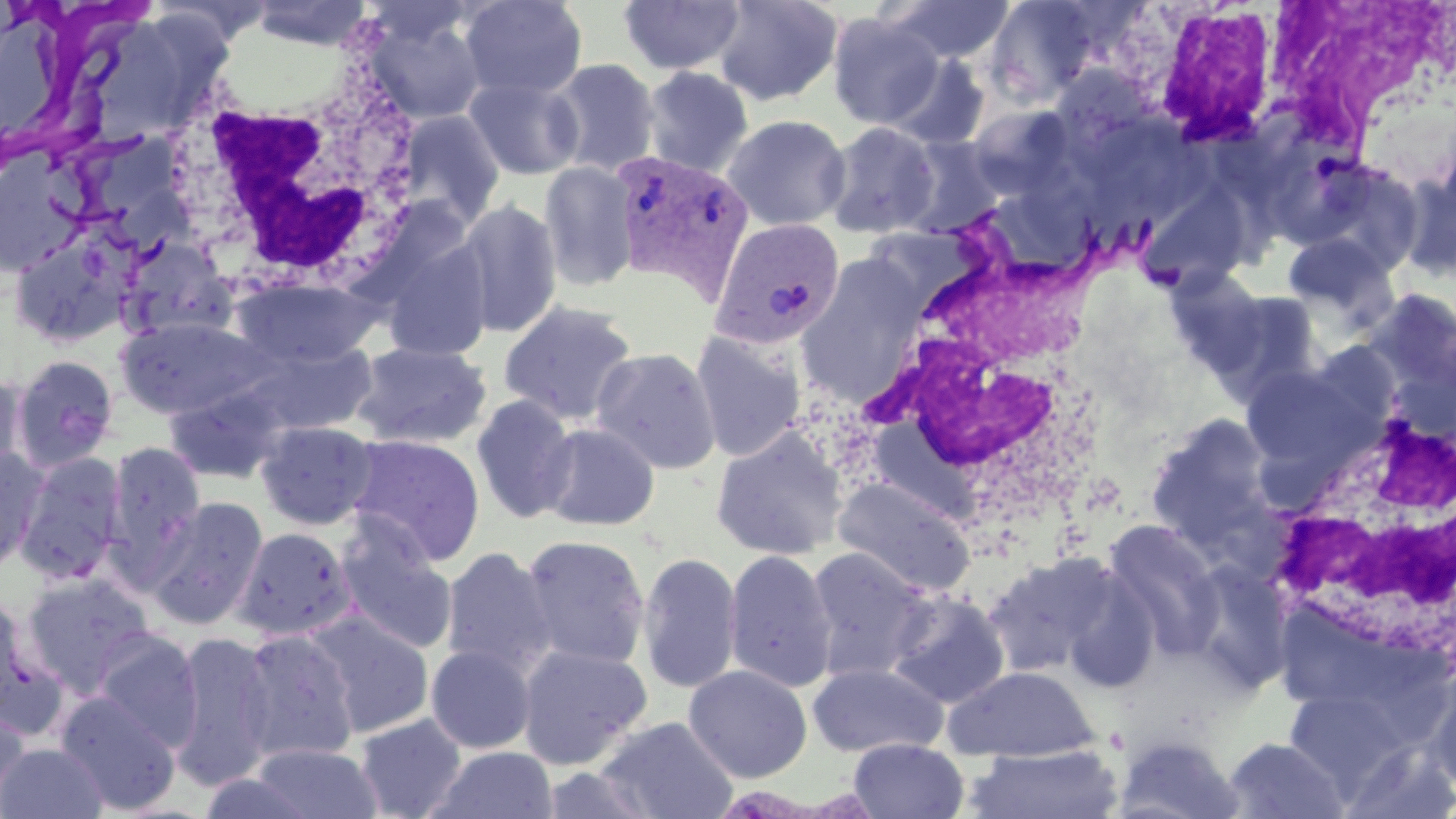 Approximate bounding boxes as named x1/y1/x2/y2 corners in pixels. Plasmodium vivax-infected red blood cell locations: (x1=610, y1=149, x2=755, y2=299), (x1=708, y1=217, x2=845, y2=352). White blood cell locations: (x1=1270, y1=3, x2=1453, y2=167), (x1=1118, y1=4, x2=1285, y2=151), (x1=159, y1=51, x2=423, y2=303), (x1=861, y1=226, x2=1112, y2=525), (x1=1261, y1=409, x2=1455, y2=662). Uninfected red blood cell locations: (x1=251, y1=0, x2=370, y2=50), (x1=460, y1=0, x2=587, y2=101), (x1=618, y1=0, x2=745, y2=76), (x1=713, y1=0, x2=844, y2=106), (x1=885, y1=0, x2=1015, y2=64), (x1=984, y1=1, x2=1104, y2=106), (x1=362, y1=9, x2=487, y2=125), (x1=3, y1=11, x2=70, y2=140), (x1=826, y1=12, x2=945, y2=130), (x1=84, y1=18, x2=184, y2=141), (x1=886, y1=54, x2=991, y2=151), (x1=547, y1=58, x2=661, y2=176), (x1=640, y1=65, x2=754, y2=179), (x1=464, y1=76, x2=584, y2=180), (x1=968, y1=105, x2=1076, y2=199), (x1=398, y1=110, x2=505, y2=226), (x1=722, y1=114, x2=850, y2=231), (x1=823, y1=122, x2=941, y2=239), (x1=903, y1=136, x2=1006, y2=237), (x1=3, y1=140, x2=92, y2=277), (x1=1308, y1=159, x2=1427, y2=276), (x1=539, y1=160, x2=639, y2=291), (x1=1135, y1=179, x2=1256, y2=295), (x1=453, y1=200, x2=563, y2=338), (x1=9, y1=231, x2=133, y2=347), (x1=1283, y1=233, x2=1397, y2=325), (x1=116, y1=237, x2=237, y2=342), (x1=382, y1=238, x2=493, y2=363), (x1=232, y1=276, x2=380, y2=368), (x1=1207, y1=288, x2=1326, y2=401), (x1=498, y1=300, x2=638, y2=426), (x1=116, y1=315, x2=267, y2=418), (x1=690, y1=331, x2=806, y2=462), (x1=244, y1=340, x2=378, y2=435), (x1=351, y1=341, x2=492, y2=449), (x1=590, y1=347, x2=723, y2=475), (x1=9, y1=354, x2=119, y2=472), (x1=1239, y1=364, x2=1365, y2=471), (x1=0, y1=371, x2=27, y2=478), (x1=164, y1=384, x2=288, y2=484), (x1=471, y1=394, x2=578, y2=524), (x1=1144, y1=412, x2=1279, y2=554), (x1=255, y1=420, x2=378, y2=529), (x1=538, y1=422, x2=661, y2=531), (x1=246, y1=423, x2=369, y2=643), (x1=710, y1=426, x2=848, y2=561), (x1=346, y1=433, x2=486, y2=566), (x1=106, y1=440, x2=206, y2=568), (x1=0, y1=447, x2=46, y2=575), (x1=13, y1=453, x2=127, y2=583), (x1=833, y1=477, x2=977, y2=597), (x1=144, y1=496, x2=268, y2=630), (x1=1100, y1=519, x2=1225, y2=658), (x1=232, y1=527, x2=357, y2=641), (x1=334, y1=527, x2=459, y2=656), (x1=519, y1=533, x2=651, y2=669), (x1=440, y1=546, x2=556, y2=678), (x1=804, y1=546, x2=937, y2=681), (x1=724, y1=548, x2=838, y2=693), (x1=981, y1=551, x2=1117, y2=676), (x1=637, y1=552, x2=742, y2=694), (x1=1183, y1=559, x2=1294, y2=692), (x1=1059, y1=564, x2=1161, y2=693), (x1=20, y1=571, x2=157, y2=696), (x1=886, y1=591, x2=1012, y2=708), (x1=0, y1=592, x2=43, y2=730), (x1=304, y1=610, x2=435, y2=739), (x1=236, y1=628, x2=361, y2=764), (x1=92, y1=630, x2=203, y2=751), (x1=168, y1=630, x2=276, y2=790), (x1=517, y1=643, x2=653, y2=769), (x1=426, y1=645, x2=536, y2=754), (x1=806, y1=662, x2=947, y2=758), (x1=683, y1=665, x2=812, y2=783), (x1=943, y1=665, x2=1098, y2=761), (x1=1426, y1=674, x2=1456, y2=792), (x1=1284, y1=691, x2=1400, y2=788), (x1=55, y1=692, x2=181, y2=814), (x1=0, y1=707, x2=32, y2=807), (x1=354, y1=713, x2=467, y2=819), (x1=595, y1=715, x2=739, y2=819), (x1=1113, y1=732, x2=1245, y2=819), (x1=1221, y1=736, x2=1350, y2=818), (x1=848, y1=738, x2=969, y2=819), (x1=1, y1=743, x2=107, y2=819), (x1=250, y1=743, x2=383, y2=819), (x1=965, y1=743, x2=1124, y2=819), (x1=430, y1=746, x2=559, y2=819), (x1=535, y1=764, x2=664, y2=819). Slide-level diagnosis: Plasmodium vivax. Thin blood film. One field of a larger specimen. Image is 1456×819 pixels. May-Grünwald-Giemsa stain. Optical microscopy. 1000x magnification.